State the blood parasite species.
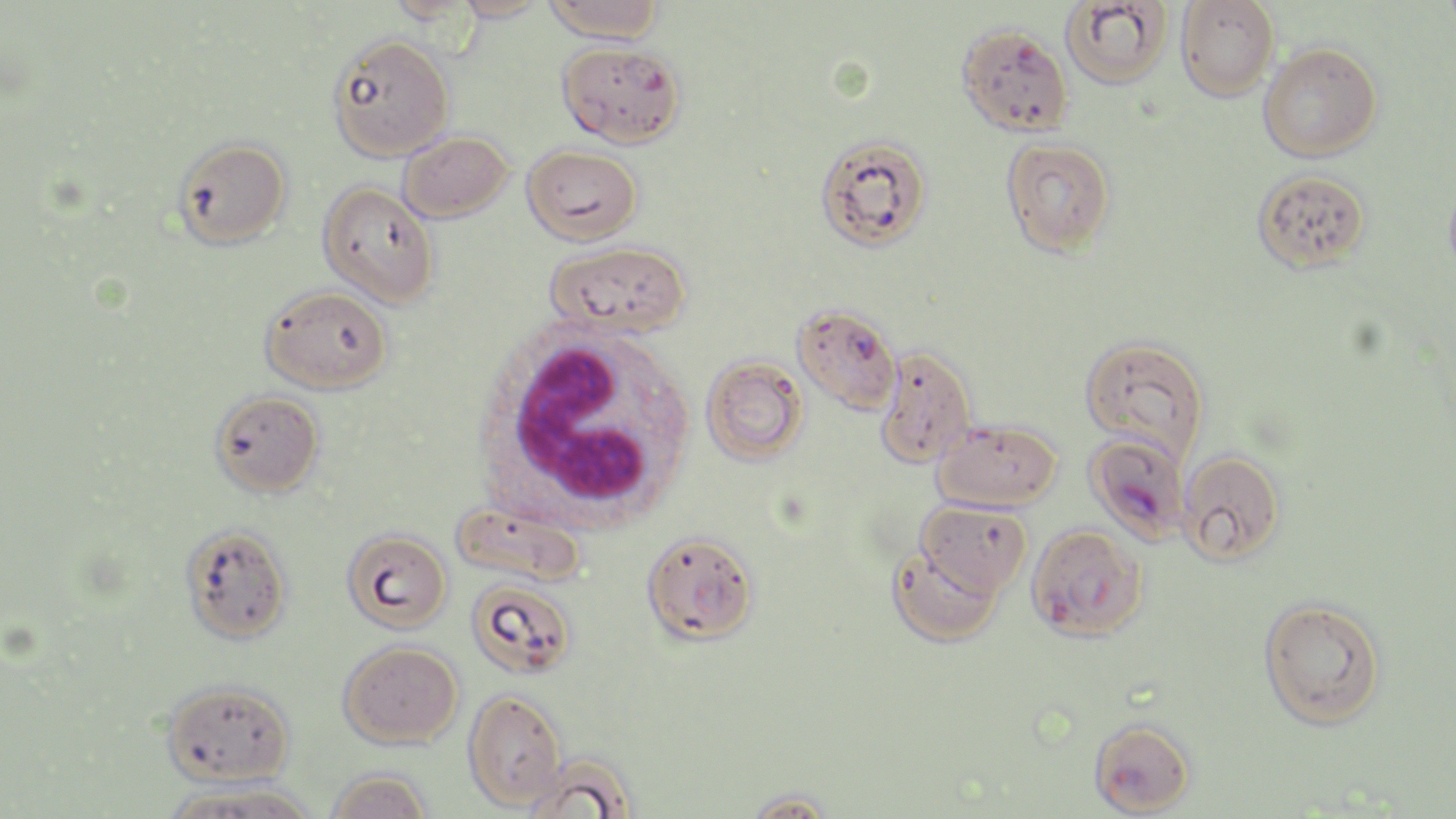

Plasmodium falciparum.

white_blood_cell_locations: 'approximate bounding boxes as (x1, y1, x2, y2) in pixels: (479, 327, 699, 527)'
magnification: 1000x
field_of_view: one of a larger specimen
stain: May-Grünwald-Giemsa
modality: optical microscopy
plasmodium_falciparum_infected_red_blood_cell_locations: 'approximate bounding boxes as (x1, y1, x2, y2) in pixels: (956, 24, 1073, 136), (557, 41, 685, 148), (1086, 432, 1192, 544), (1026, 523, 1148, 642), (641, 531, 759, 644), (1088, 717, 1196, 816)'
image_size: 1456×819 pixels
preparation: thin blood smear
uninfected_red_blood_cell_locations: 'approximate bounding boxes as (x1, y1, x2, y2) in pixels: (385, 0, 479, 23), (453, 0, 549, 22), (543, 0, 663, 43), (1176, 0, 1278, 101), (1061, 1, 1172, 89), (329, 34, 454, 161), (1259, 42, 1381, 162), (399, 131, 513, 221), (173, 136, 291, 249), (815, 136, 934, 252), (1001, 137, 1116, 258), (522, 144, 642, 245), (1252, 169, 1371, 274), (1443, 171, 1456, 286), (317, 180, 439, 307), (547, 241, 691, 337), (260, 284, 392, 394), (793, 304, 902, 414), (1079, 334, 1210, 462), (874, 346, 976, 469), (702, 356, 808, 465), (210, 389, 324, 497), (933, 419, 1061, 512), (1178, 449, 1285, 566), (449, 497, 588, 588), (917, 500, 1032, 596), (181, 524, 293, 644), (341, 527, 453, 633), (887, 546, 1002, 647), (468, 580, 576, 679), (1258, 597, 1386, 730), (338, 640, 462, 749), (162, 679, 295, 787), (463, 689, 566, 811), (521, 757, 634, 819), (325, 770, 432, 819), (163, 780, 320, 819), (741, 789, 841, 819)'